Classify this cell by malaria status.
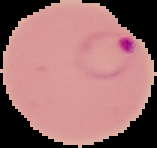
It is parasitized.

{
  "preparation": "thin blood smear",
  "image_type": "segmented cell region on a black background",
  "image_size": "157×148 pixels"
}